Point out leukocytes.
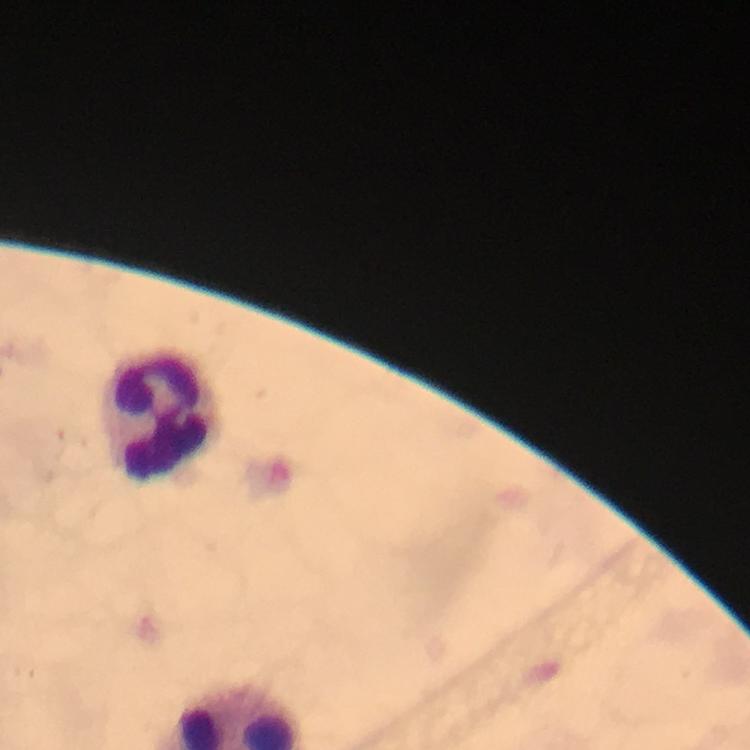
Approximate object centers, in pixels from the top-left corner.
Leukocytes: (x=165, y=412).

Summary:
  - Cropped from: a single field of view
  - Immersion oil: used
  - Context: from a malaria diagnostic workup
  - Magnification: 100x
  - Capture: smartphone mounted on the microscope
  - Preparation: thick blood smear
  - Image size: 750×750 pixels
  - Plasmodium parasites: none detected
  - Stain: Giemsa